Locate every Plasmodium parasite.
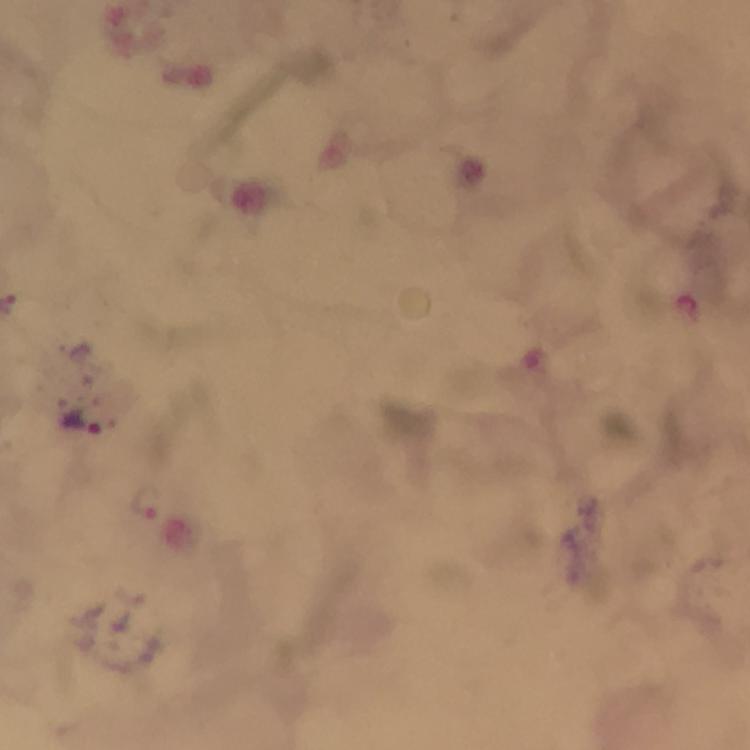
Approximate centers as (x, y) in pixels.
Plasmodium parasites: (82, 421), (148, 501).

Image is 750×750 pixels. Immersion oil applied. At 100x magnification. Photographed through the microscope with a smartphone camera. From a malaria diagnostic workup. Cropped region of a single field of view. Giemsa stain. Thick smear.